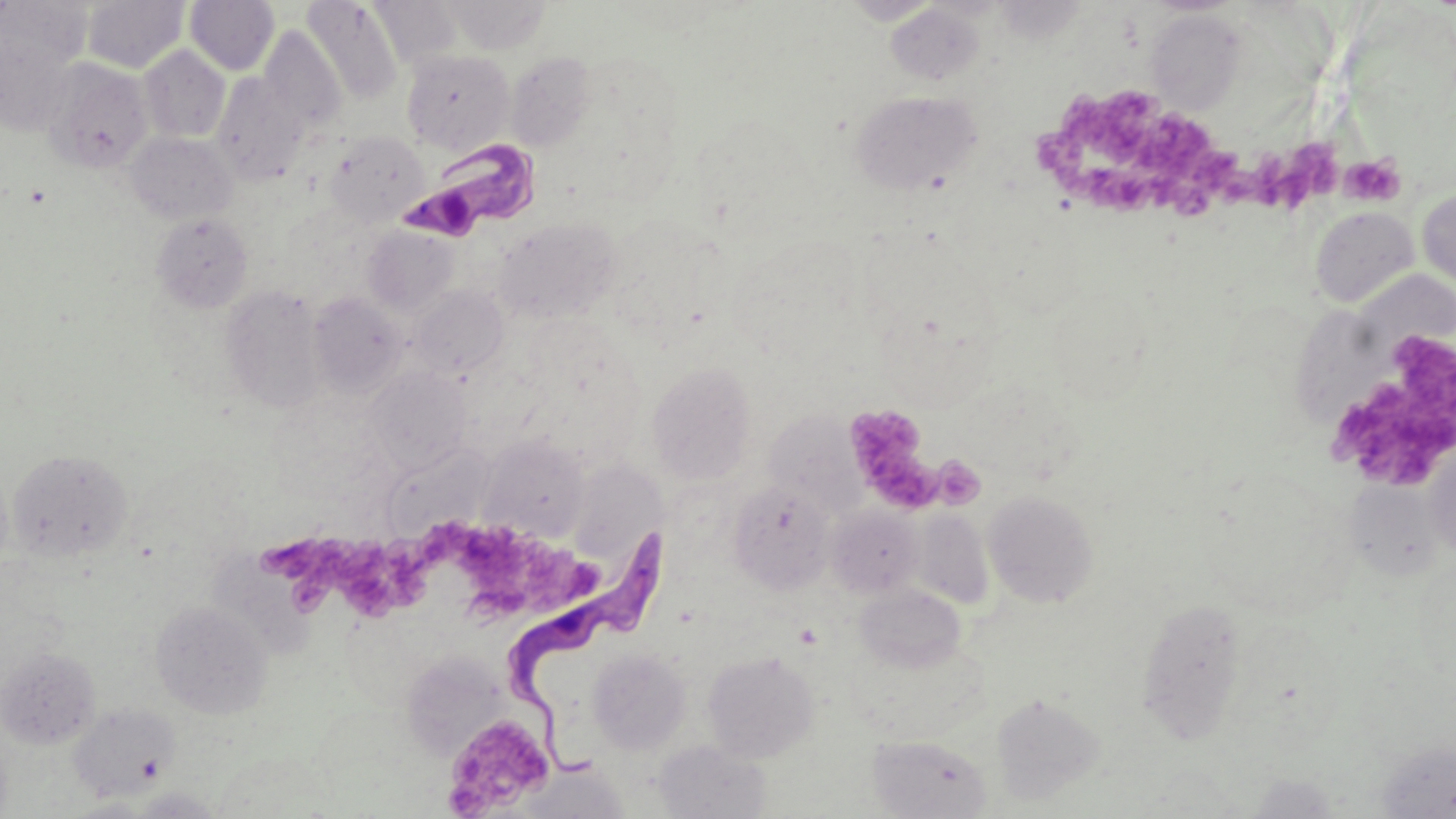
Approximate bounding boxes as (x1,y1)-(x2,y2) corner pairs in pixels. Uninfected red blood cell locations: (82,0)-(189,73), (184,0)-(279,75), (367,0)-(466,71), (444,0)-(551,54), (1,1)-(93,75), (302,1)-(403,104), (886,4)-(987,84), (1146,10)-(1246,114), (259,25)-(347,134), (0,34)-(76,136), (139,45)-(230,143), (401,48)-(515,153), (505,52)-(596,152), (42,58)-(154,173), (211,73)-(309,184), (849,89)-(982,194), (325,130)-(430,227), (126,131)-(238,224), (1417,188)-(1456,292), (1310,206)-(1419,307), (151,213)-(254,313), (493,217)-(622,324), (362,226)-(461,318), (221,285)-(327,413), (411,286)-(508,379), (308,292)-(409,397), (1300,309)-(1397,419), (647,361)-(757,484), (364,367)-(472,473), (765,412)-(864,515), (481,437)-(590,539), (1424,440)-(1456,559), (380,444)-(490,539), (6,449)-(134,563), (572,452)-(670,569), (729,482)-(835,594), (983,489)-(1099,608), (827,504)-(922,598), (907,507)-(994,609), (213,545)-(318,663), (855,585)-(969,673), (1135,596)-(1250,744), (151,601)-(272,718), (0,646)-(101,749), (588,647)-(691,754), (702,650)-(819,763), (405,651)-(507,769), (990,692)-(1105,805), (68,703)-(180,802), (868,734)-(992,818), (653,739)-(771,818), (1376,740)-(1456,815), (517,762)-(630,818), (1245,773)-(1342,817), (125,787)-(227,818). Platelet locations: (1070,88)-(1240,188), (1031,124)-(1101,203), (1239,140)-(1342,215), (1339,154)-(1405,208), (1087,167)-(1215,219), (1318,319)-(1456,494), (843,404)-(935,504), (934,458)-(989,513), (458,525)-(598,617), (264,529)-(429,615), (448,718)-(551,817). Trypanosoma brucei locations: (396,139)-(543,243), (505,528)-(676,782). Slide-level diagnosis: Trypanosoma brucei. May-Grünwald-Giemsa-stained preparation. Optical microscopy. Captured at 1000x magnification. Thin blood film. One field of a larger specimen. Image is 1456×819 pixels.